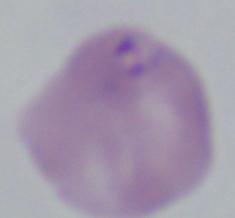

A Babesia parasite is seen. 1000x magnification. Micrograph.